Outline each blood parasite and name the species.
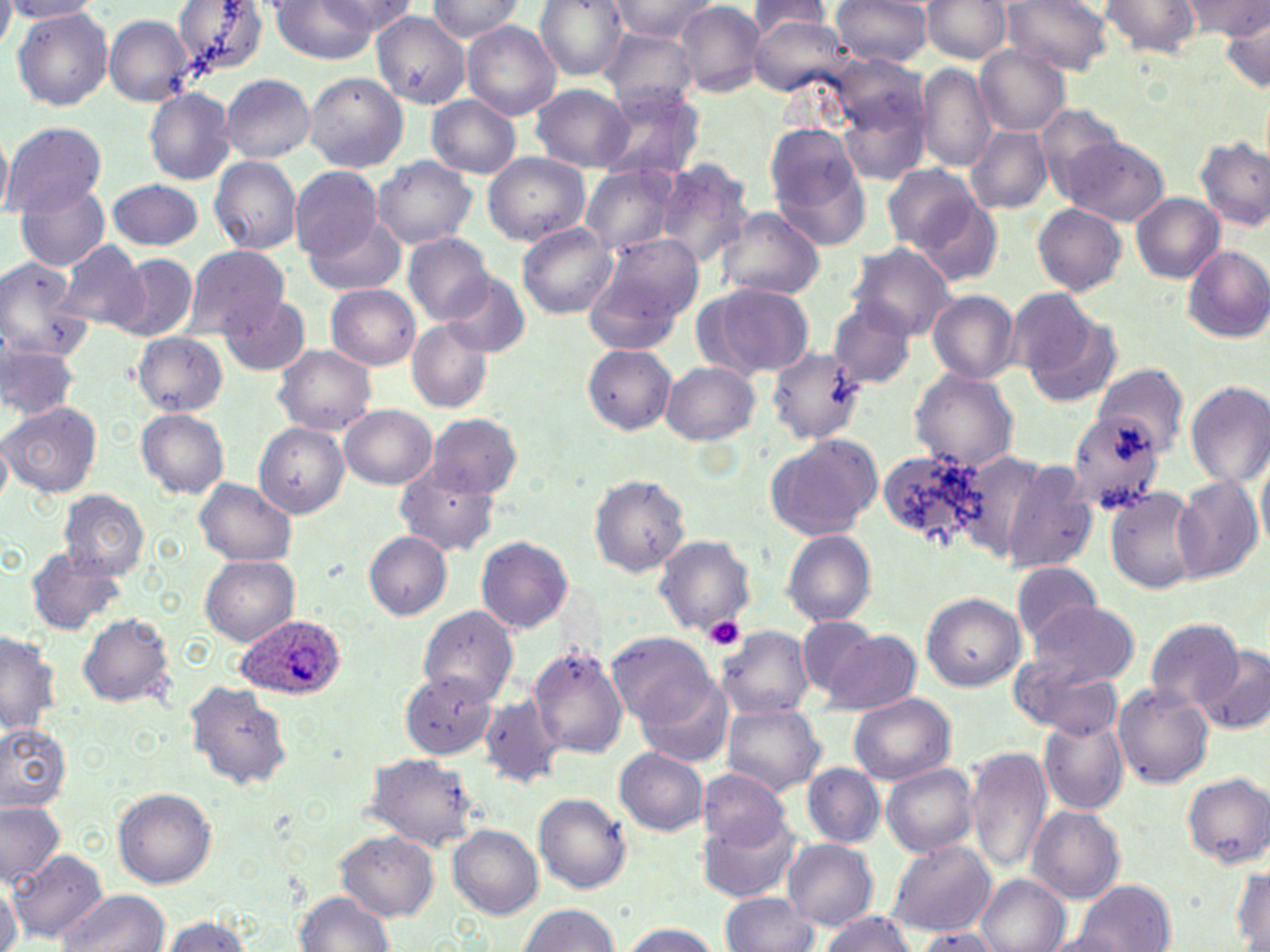

Approximate bounding boxes as (x1, y1, x2, y2) in pixels.
Plasmodium ovale-infected red blood cells: (235, 616, 345, 696).
No Plasmodium falciparum, Plasmodium malariae, Plasmodium vivax, Babesia divergens, or Trypanosoma brucei observed.

Uninfected red blood cell locations: (3, 0, 100, 21), (172, 0, 271, 75), (264, 0, 405, 64), (424, 0, 523, 43), (534, 0, 627, 82), (612, 0, 718, 42), (831, 0, 931, 69), (925, 0, 1011, 64), (1007, 0, 1112, 77), (1098, 0, 1201, 59), (1184, 0, 1270, 40), (748, 1, 831, 38), (676, 3, 764, 96), (12, 8, 116, 111), (373, 12, 470, 112), (103, 14, 195, 107), (748, 16, 855, 100), (1218, 16, 1269, 95), (464, 22, 561, 120), (603, 27, 698, 113), (976, 45, 1069, 138), (917, 63, 995, 171), (305, 69, 407, 173), (221, 75, 316, 163), (531, 85, 633, 172), (605, 85, 703, 179), (836, 85, 930, 185), (146, 87, 236, 185), (426, 95, 522, 178), (6, 124, 106, 219), (965, 125, 1052, 216), (767, 126, 872, 249), (1196, 133, 1270, 229), (1052, 135, 1171, 227), (1, 136, 15, 216), (484, 153, 590, 246), (210, 155, 300, 254), (374, 157, 475, 250), (657, 161, 756, 276), (581, 165, 676, 260), (881, 168, 981, 254), (292, 170, 383, 266), (106, 177, 204, 250), (15, 183, 110, 270), (1131, 191, 1226, 282), (912, 197, 1004, 287), (1032, 204, 1125, 295), (717, 205, 825, 303), (306, 216, 406, 296), (517, 223, 616, 317), (404, 236, 492, 326), (582, 236, 704, 350), (59, 240, 149, 329), (854, 243, 956, 341), (1182, 247, 1270, 345), (186, 249, 289, 335), (0, 254, 85, 365), (107, 254, 198, 344), (439, 273, 530, 358), (327, 284, 421, 371), (693, 284, 815, 381), (928, 293, 1019, 385), (220, 294, 312, 375), (1016, 300, 1121, 406), (828, 301, 914, 392), (409, 320, 493, 413), (132, 332, 229, 416), (767, 342, 867, 448), (2, 343, 77, 420), (585, 344, 676, 436), (275, 345, 376, 437), (661, 361, 759, 447), (1095, 364, 1187, 452), (911, 367, 1017, 474), (1185, 382, 1270, 489), (3, 401, 103, 499), (340, 405, 437, 491), (1069, 408, 1168, 519), (137, 410, 229, 499), (428, 417, 523, 498), (256, 422, 354, 517), (766, 435, 882, 541), (875, 447, 991, 554), (950, 450, 1053, 559), (996, 457, 1098, 570), (396, 469, 500, 555), (588, 473, 689, 579), (1170, 473, 1263, 583), (196, 477, 294, 565), (1105, 486, 1200, 593), (59, 490, 148, 582), (364, 530, 452, 619), (784, 531, 876, 627), (651, 537, 754, 633), (476, 538, 572, 632), (25, 544, 126, 631), (199, 554, 299, 647), (1011, 564, 1100, 650), (922, 592, 1026, 692), (1030, 603, 1138, 688), (417, 606, 518, 706), (80, 610, 177, 707), (1144, 617, 1245, 715), (797, 618, 875, 699), (720, 627, 813, 723), (0, 630, 60, 738), (825, 630, 922, 714), (610, 634, 716, 727), (529, 645, 628, 760), (1198, 648, 1270, 735), (401, 668, 493, 757), (1036, 670, 1123, 738), (187, 680, 291, 793), (639, 680, 737, 769), (1114, 681, 1214, 789), (849, 695, 956, 785), (480, 697, 563, 787), (722, 700, 824, 796), (1040, 714, 1130, 815), (0, 724, 71, 812), (613, 745, 707, 834), (966, 746, 1050, 875), (363, 752, 482, 849), (882, 763, 979, 860), (804, 764, 884, 848), (695, 766, 789, 845), (1183, 774, 1270, 869), (115, 789, 216, 889), (533, 791, 631, 895), (0, 801, 65, 887), (1028, 807, 1123, 904), (697, 818, 803, 900), (450, 825, 543, 918), (336, 832, 438, 918), (784, 839, 878, 932), (889, 839, 995, 936), (9, 852, 107, 945), (1230, 859, 1269, 950), (977, 874, 1071, 952), (1, 876, 19, 952), (1065, 880, 1176, 952), (56, 888, 170, 952), (292, 888, 399, 952), (723, 893, 818, 952), (517, 903, 623, 952), (818, 911, 918, 952), (159, 912, 257, 952), (619, 920, 726, 952), (911, 927, 1008, 952). Platelet locations: (704, 617, 744, 653). Slide-level diagnosis: Plasmodium ovale. Thin blood smear. May-Grünwald-Giemsa stain. Image is 1270×952 pixels. Light microscopy. One field of a larger specimen. Captured at 1000x magnification.